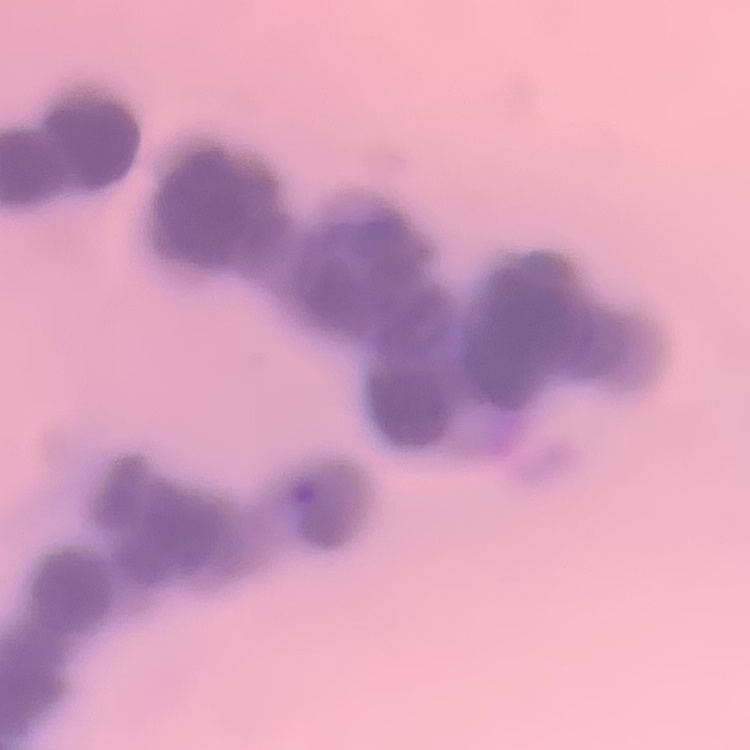

Summary:
  - Red blood cell morphology: rouleaux formation
  - Stain: Field's or Giemsa
  - Preparation: thin peripheral smear
  - Image type: one tile cut from a larger photomicrograph